Assess this cell for malaria.
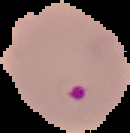
Parasitized.

image type = cell region segmented out of the field of view; surrounding area masked to black
preparation = thin blood film
image size = 130×133 pixels